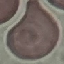
Result: no malaria parasites seen. Photographed with a smartphone camera at the microscope eyepiece. Cell patch, automatically extracted from a larger field of view and resized to 64 × 64 pixels. Giemsa-stained preparation. Thin blood film.